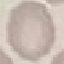

Summary:
  - Result: no malaria parasites seen
  - Image type: automatically extracted cell patch, resized to 64 × 64 pixels
  - Stain: Giemsa
  - Preparation: thin smear
  - Capture: smartphone camera at the microscope eyepiece